Point out each leukocyte.
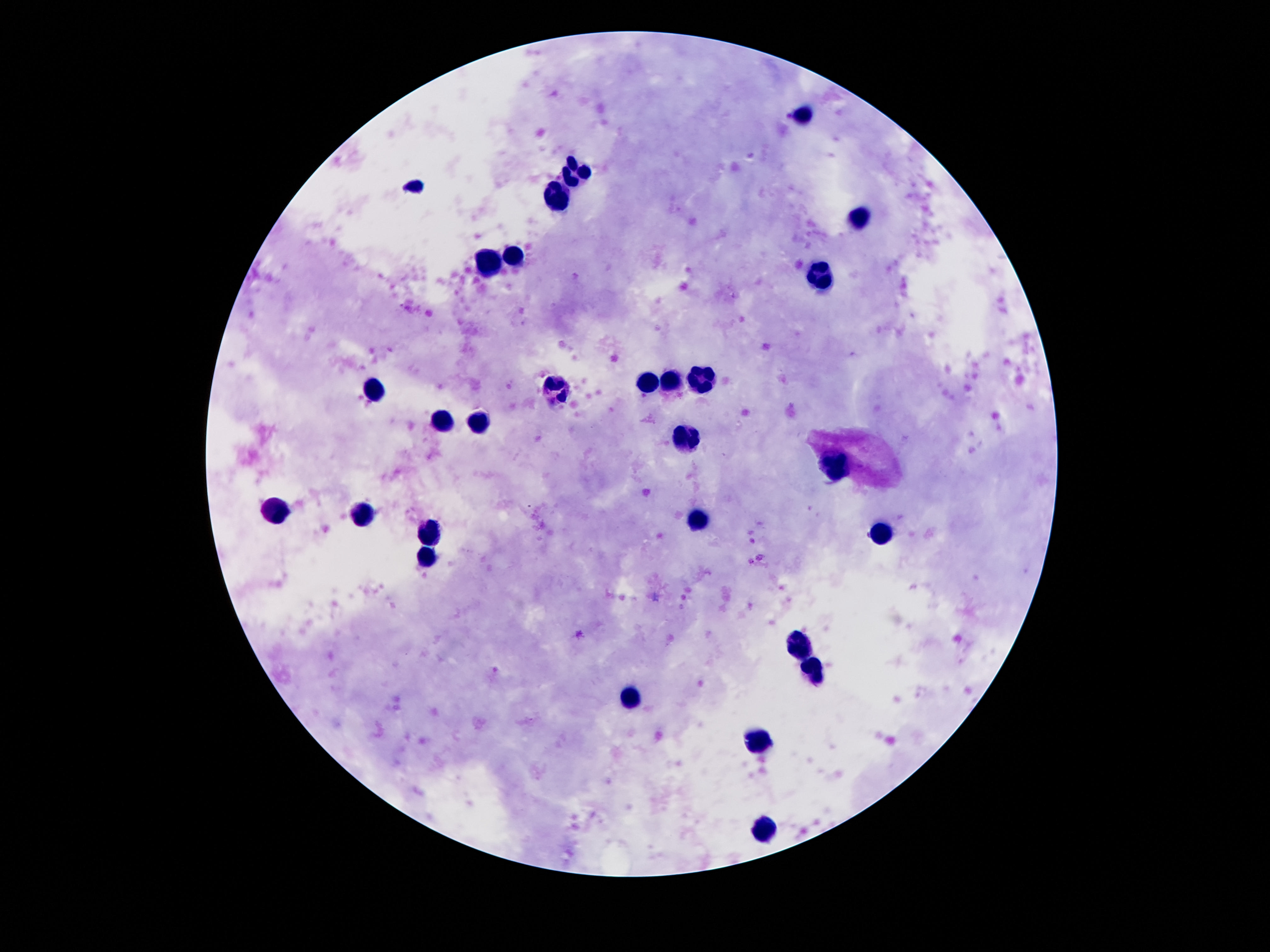

Approximate object centers, in pixels from the top-left corner.
Leukocytes: (x=806, y=113), (x=572, y=174), (x=556, y=199), (x=855, y=219), (x=513, y=253), (x=488, y=265), (x=820, y=277), (x=671, y=381), (x=701, y=382), (x=644, y=385), (x=370, y=390), (x=554, y=392), (x=439, y=421), (x=478, y=424), (x=685, y=441), (x=829, y=468), (x=275, y=515), (x=363, y=515), (x=699, y=521), (x=429, y=534), (x=880, y=534), (x=427, y=558), (x=800, y=644), (x=812, y=670), (x=630, y=698), (x=757, y=741), (x=765, y=830).

Thick blood smear. Smartphone photograph taken through the microscope eyepiece. Single field of view. Patient malaria status: uninfected. Giemsa-stained preparation. 100x magnification. Image is 1270×952 pixels.